Classify this cell by malaria status.
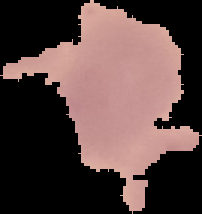
It is uninfected.

Summary:
  - Preparation: thin blood film
  - Image type: segmented cell region on a black background
  - Image size: 202×214 pixels